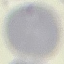
Summary:
  - Malaria status: uninfected
  - Image type: cell patch, automatically extracted from a larger field of view and resized to 64 × 64 pixels
  - Stain: Giemsa
  - Preparation: thin blood smear
  - Capture: smartphone camera at the microscope eyepiece